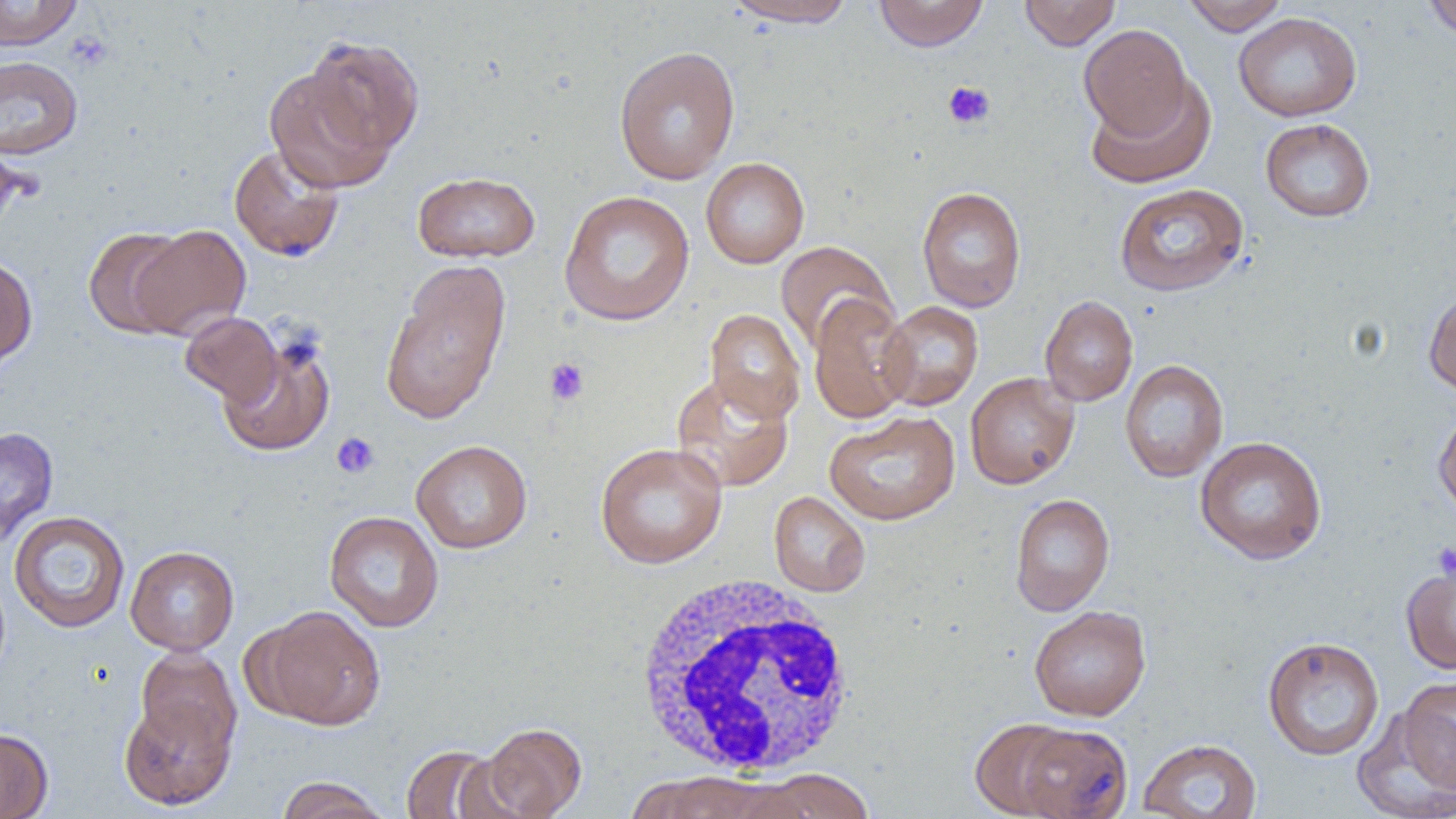
slide_level_diagnosis: negative for blood parasites
platelet_locations: 'approximate bounding boxes as (x1, y1, x2, y2) in pixels: (67, 32, 113, 71), (942, 80, 996, 130), (544, 357, 590, 406), (331, 432, 380, 479), (1432, 541, 1456, 579)'
uninfected_red_blood_cell_locations: 'approximate bounding boxes as (x1, y1, x2, y2) in pixels: (0, 0, 84, 50), (723, 0, 856, 28), (873, 0, 989, 51), (1018, 0, 1121, 50), (1182, 0, 1289, 35), (1421, 0, 1456, 40), (1232, 12, 1362, 122), (1079, 24, 1193, 140), (305, 36, 424, 157), (613, 46, 741, 185), (0, 56, 83, 160), (264, 67, 398, 194), (1085, 74, 1216, 189), (1260, 118, 1375, 222), (0, 137, 30, 249), (228, 143, 345, 261), (700, 157, 809, 268), (412, 171, 540, 263), (1114, 182, 1249, 297), (916, 186, 1027, 313), (559, 190, 695, 325), (130, 224, 251, 341), (83, 227, 190, 339), (775, 240, 895, 353), (0, 253, 38, 370), (381, 261, 511, 424), (1423, 285, 1456, 395), (807, 293, 916, 424), (1039, 295, 1138, 407), (877, 301, 984, 411), (705, 308, 806, 423), (180, 311, 282, 406), (217, 331, 337, 457), (1120, 359, 1229, 482), (670, 370, 794, 492), (964, 372, 1080, 489), (1433, 408, 1456, 520), (824, 410, 960, 525), (0, 426, 58, 549), (1194, 435, 1328, 564), (411, 439, 532, 553), (594, 441, 728, 569), (769, 491, 870, 598), (1009, 493, 1115, 616), (9, 510, 130, 633), (324, 510, 444, 632), (125, 545, 239, 655), (1400, 567, 1456, 673), (255, 605, 387, 730), (1029, 605, 1151, 721), (1262, 636, 1385, 761), (134, 648, 242, 760), (1398, 676, 1456, 793), (118, 692, 238, 810), (1352, 707, 1456, 819), (969, 718, 1079, 818), (478, 722, 587, 819), (1012, 722, 1134, 818), (0, 727, 54, 819), (1137, 738, 1262, 818), (398, 744, 515, 819), (744, 768, 874, 819), (629, 770, 768, 819), (274, 776, 393, 819)'
magnification: 1000x
preparation: thin blood smear
image_size: 1456×819 pixels
modality: light microscopy
field_of_view: one of a larger specimen
white_blood_cell_locations: 'approximate bounding boxes as (x1, y1, x2, y2) in pixels: (630, 572, 857, 779)'